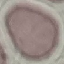 Result: no malaria parasites detected. Acquired by smartphone through the microscope eyepiece. Cell patch, automatically extracted from a larger field of view and resized to 64 × 64 pixels. Giemsa stain. Thin blood smear.